Describe the morphology of the erythrocytes.
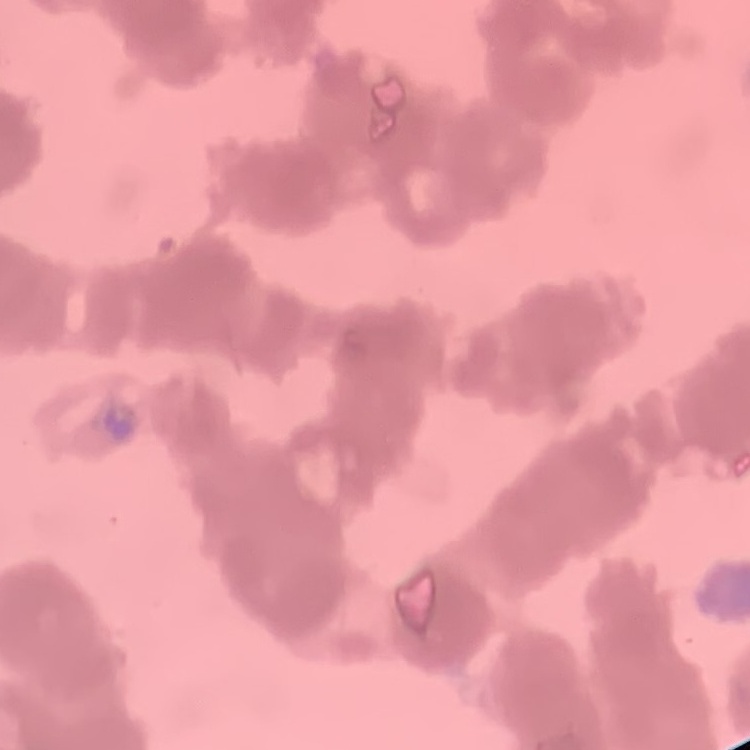
Rouleaux formation.

Summary:
  - Image type: one tile cut from a larger photomicrograph
  - Stain: Field's or Giemsa
  - Preparation: thin blood smear